Assess this cell for malaria.
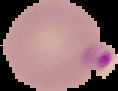

Parasitized.

Summary:
  - Image size: 118×91 pixels
  - Preparation: thin blood smear
  - Image type: segmented cell region on a black background